Assess the morphology of the erythrocytes.
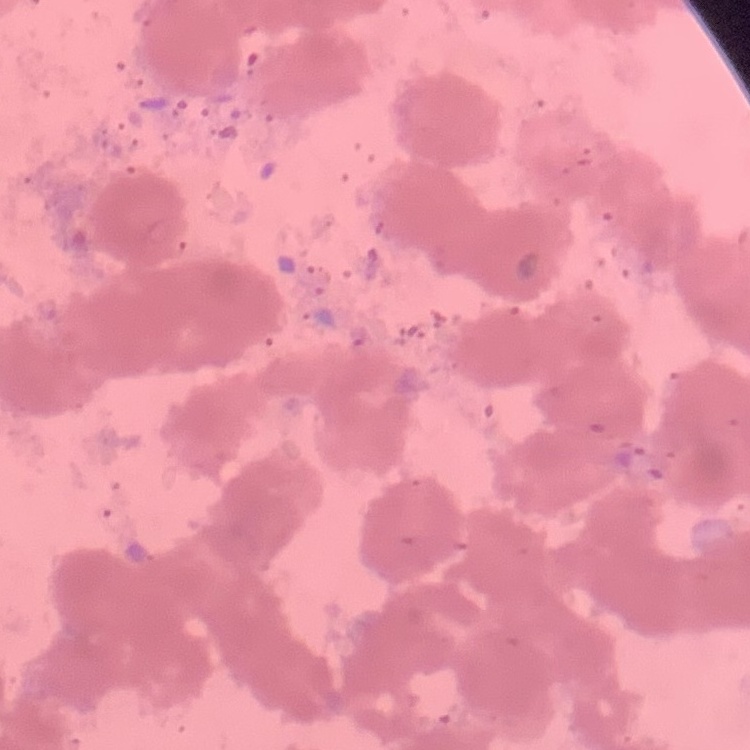
Rouleaux formation.

Field's or Giemsa stain. One tile cut from a larger photomicrograph. Thin blood smear.